Identify the parasite.
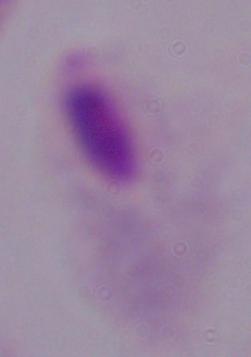
A trichomonad.

{
  "modality": "photomicrograph",
  "magnification": "1000x"
}